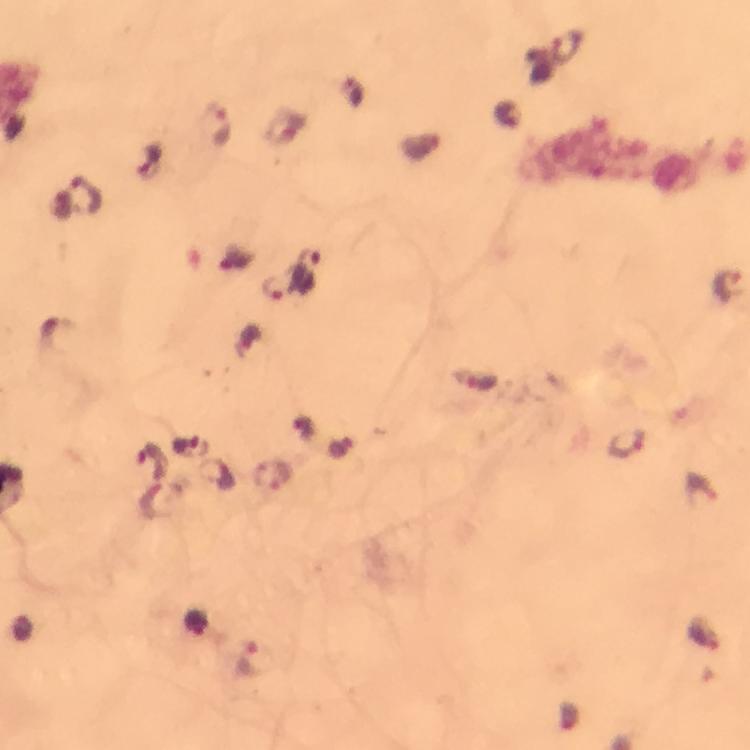
preparation: thick blood smear
image_size: 750×750 pixels
context: from a malaria diagnostic workup
plasmodium_parasite_locations: 'approximate centers as [x, y] in pixels: [216, 126], [307, 267], [726, 284], [273, 286], [474, 381], [628, 444], [273, 475], [255, 660]'
immersion_oil: applied
capture: smartphone photograph through a microscope
magnification: 100x
cropped_from: a single field of view
stain: Giemsa